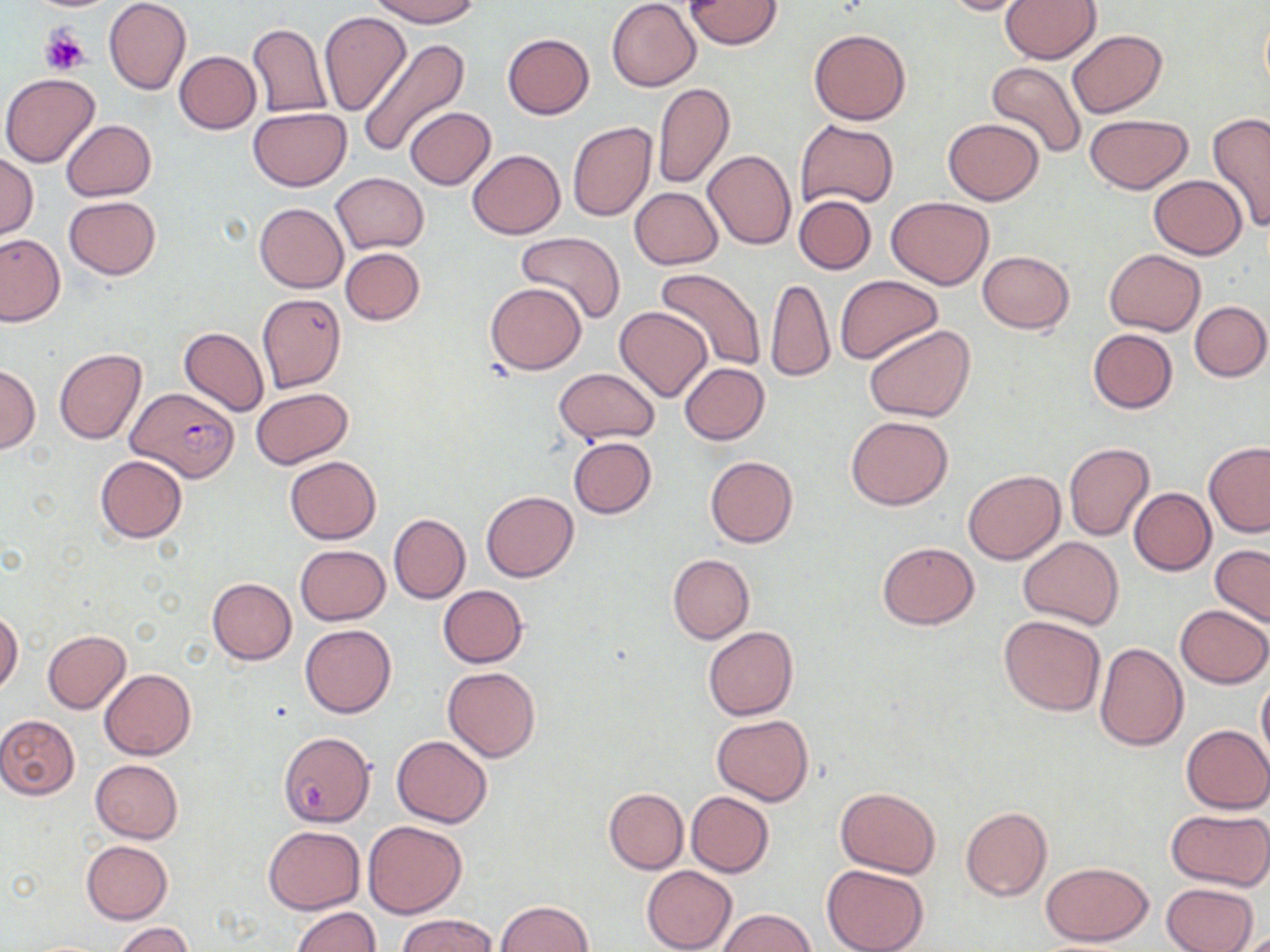
slide-level diagnosis = Plasmodium falciparum
uninfected red blood cell locations = approximate bounding boxes as (x1, y1, x2, y2) in pixels: (104, 0, 191, 95), (367, 0, 480, 26), (607, 0, 700, 91), (685, 0, 783, 49), (935, 0, 1040, 17), (1000, 0, 1101, 63), (320, 11, 411, 115), (247, 22, 332, 118), (809, 28, 910, 124), (1067, 29, 1166, 119), (502, 33, 595, 119), (357, 37, 470, 160), (174, 51, 261, 133), (985, 60, 1087, 159), (1, 73, 101, 168), (652, 82, 733, 189), (404, 107, 495, 189), (247, 108, 350, 191), (1207, 113, 1270, 230), (1083, 114, 1193, 194), (942, 118, 1044, 205), (61, 119, 156, 199), (795, 119, 900, 209), (567, 122, 656, 221), (467, 149, 565, 239), (703, 150, 797, 249), (0, 153, 38, 239), (329, 172, 429, 253), (1148, 175, 1247, 259), (629, 187, 723, 269), (794, 194, 877, 274), (64, 196, 161, 279), (887, 197, 995, 289), (253, 203, 348, 293), (515, 232, 626, 325), (0, 233, 65, 326), (341, 247, 424, 325), (1105, 248, 1205, 335), (978, 251, 1074, 332), (655, 271, 766, 372), (835, 276, 942, 364), (764, 277, 835, 381), (485, 283, 587, 375), (257, 293, 347, 393), (1190, 300, 1269, 382), (614, 306, 713, 401), (863, 325, 974, 422), (180, 327, 269, 416), (1087, 329, 1178, 413), (55, 348, 145, 444), (680, 363, 769, 444), (0, 365, 40, 453), (552, 367, 661, 444), (251, 387, 353, 469), (846, 416, 953, 510), (567, 437, 656, 517), (1064, 442, 1154, 541), (1203, 442, 1270, 536), (95, 454, 188, 542), (284, 456, 381, 544), (705, 456, 798, 548), (962, 470, 1064, 564), (1129, 488, 1215, 575), (481, 491, 577, 581), (389, 513, 470, 604), (1019, 536, 1124, 629), (877, 542, 979, 628), (295, 544, 390, 624), (1210, 544, 1270, 628), (667, 554, 754, 643), (208, 578, 296, 664), (437, 585, 528, 668), (1176, 605, 1270, 688), (0, 610, 24, 694), (999, 616, 1106, 715), (300, 623, 396, 718), (1016, 624, 1174, 728), (702, 626, 798, 720), (43, 630, 130, 713), (1095, 642, 1189, 751), (443, 666, 540, 762), (99, 668, 195, 760), (1257, 675, 1270, 766), (0, 715, 80, 800), (711, 715, 813, 804), (1180, 724, 1270, 813), (392, 735, 491, 828), (89, 759, 183, 843), (835, 787, 941, 877), (604, 788, 687, 874), (686, 791, 775, 877), (960, 807, 1051, 900), (1165, 809, 1270, 890), (363, 820, 467, 918), (263, 825, 365, 914), (82, 841, 173, 923), (1042, 862, 1152, 945), (822, 864, 929, 952), (642, 866, 737, 952), (1162, 881, 1259, 952), (497, 900, 592, 951), (291, 906, 380, 952), (719, 909, 815, 951), (398, 914, 497, 951), (115, 922, 195, 952)
Plasmodium falciparum-infected red blood cell locations = approximate bounding boxes as (x1, y1, x2, y2) in pixels: (127, 387, 238, 487), (281, 734, 375, 827)
modality = optical microscopy
preparation = thin blood film
platelet locations = approximate bounding boxes as (x1, y1, x2, y2) in pixels: (41, 27, 90, 76)
stain = May-Grünwald-Giemsa
image size = 1270×952 pixels
field of view = single
magnification = 1000x